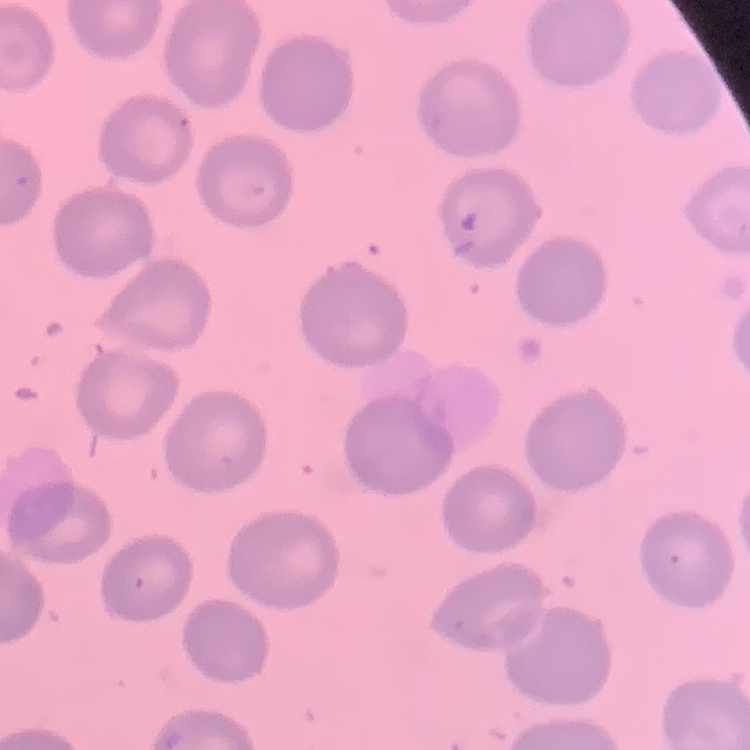
{
  "red_blood_cell_morphology": "no rouleaux formation",
  "stain": "Field's or Giemsa",
  "image_type": "square crop of a larger photomicrograph",
  "preparation": "thin blood smear"
}